Assess the morphology of the erythrocytes.
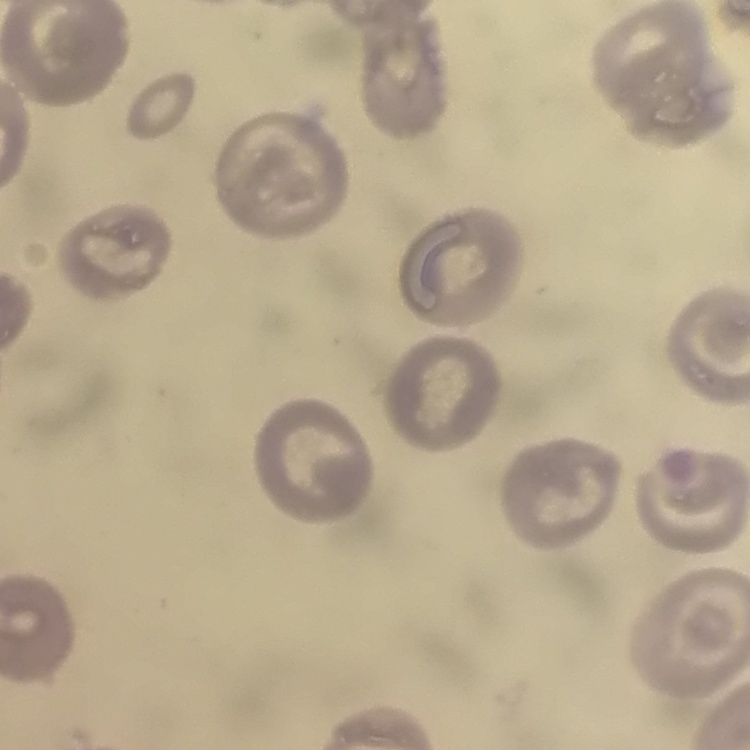

No rouleaux formation.

One tile cut from a larger photomicrograph. Field's or Giemsa stain. Thin blood smear.